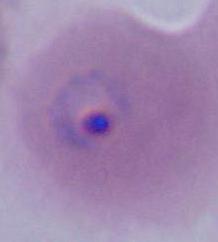
magnification = 400x or 1000x
modality = micrograph
identification = Plasmodium